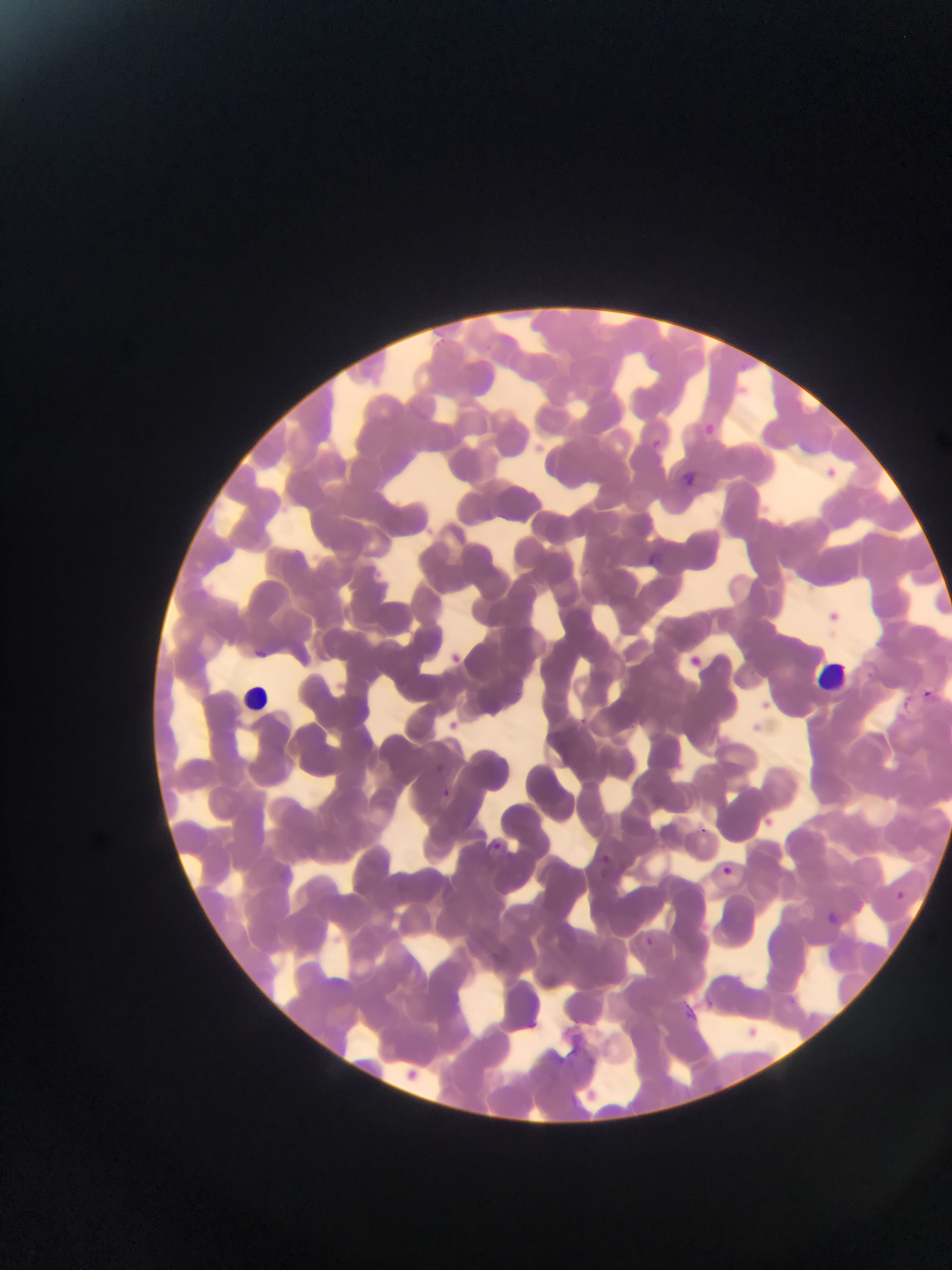

Approximate bounding boxes as (left, top, right, bottom) in pixels.
Summary:
  - Leukocyte locations: (817, 658, 865, 702), (246, 671, 291, 713)
  - Plasmodium parasite locations: (680, 472, 698, 489), (644, 554, 661, 570), (515, 690, 525, 699), (922, 690, 932, 699), (579, 715, 585, 725), (631, 722, 640, 732), (440, 787, 452, 798), (700, 826, 716, 834), (490, 840, 505, 854), (597, 855, 612, 871), (722, 866, 733, 877), (892, 889, 906, 902), (824, 910, 839, 926), (644, 937, 655, 948), (782, 993, 800, 1010), (678, 1004, 700, 1025) | approximate (x, y) pixel centers of objects too small to bound: (631, 760)
  - Image size: 952×1270 pixels
  - Country: Ghana
  - Capture: mobile-phone photograph through a microscope
  - Preparation: thin blood smear
  - Field of view: single